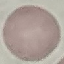 Result: no malaria parasites detected. Photographed with a smartphone camera at the microscope eyepiece. Thin blood smear. Cell patch, automatically extracted from a larger field of view and resized to 64 × 64 pixels. Giemsa stain.